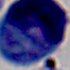

Photomicrograph. A white blood cell is seen. 1000x magnification.